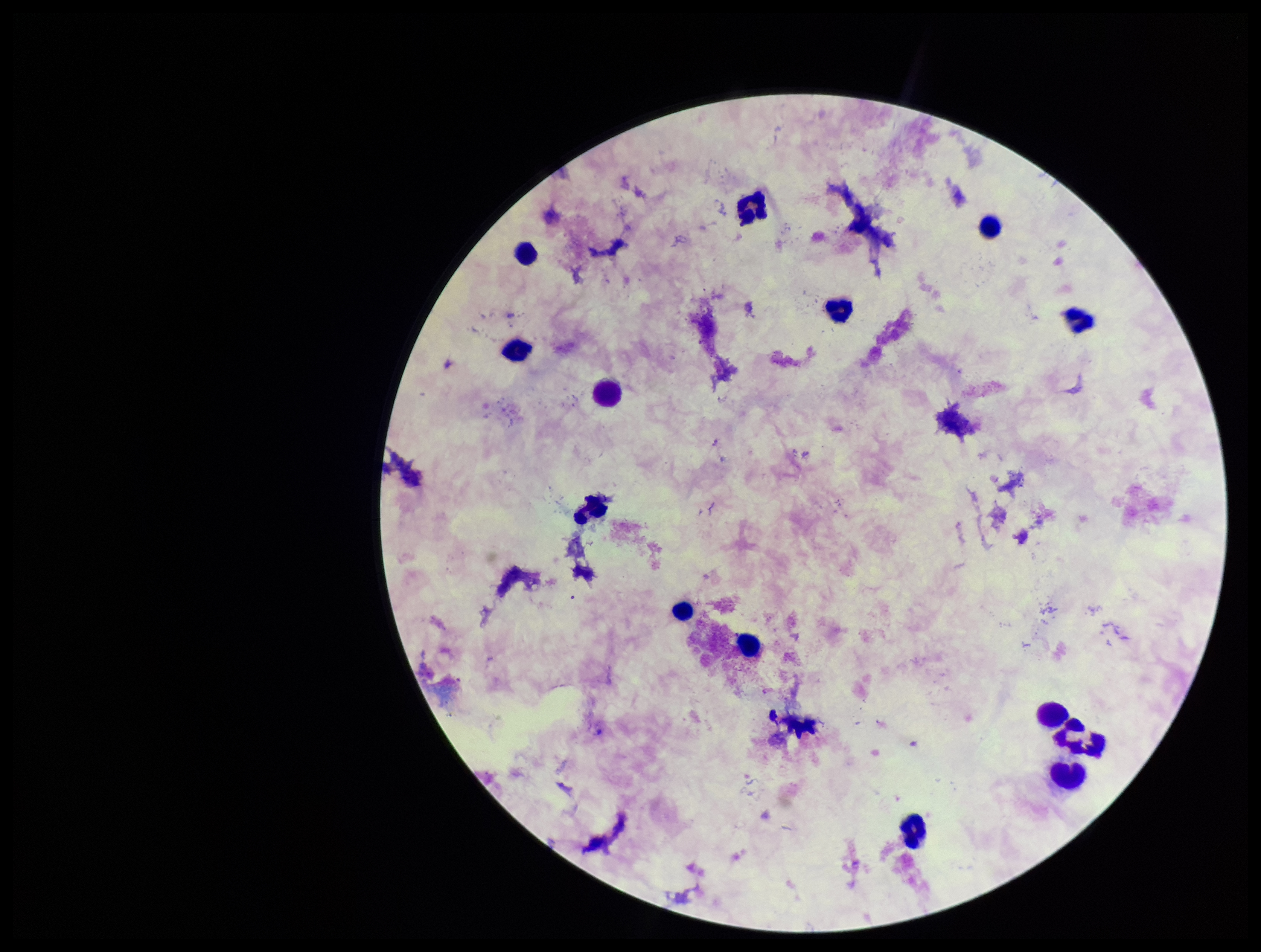
image size = 1261×952 pixels
capture = smartphone photograph through the microscope eyepiece
parasite count = 0
stain = Giemsa
Plasmodium parasites = none detected
preparation = thick
leukocyte count = 14
patient malaria status = negative
field of view = one from this slide